Assess the morphology of the erythrocytes.
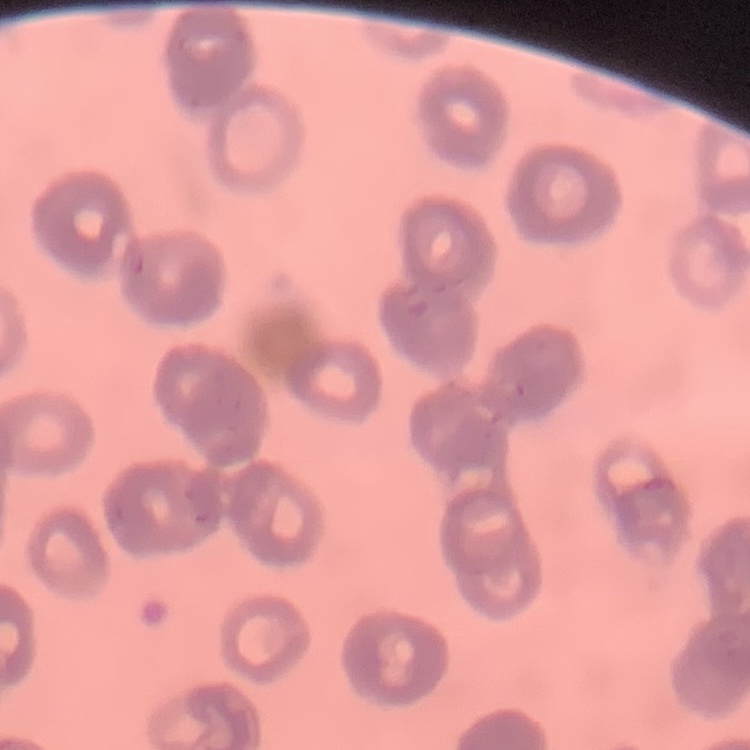
They show rouleaux formation.

image_type: square crop of a larger photomicrograph
preparation: thin blood film
stain: Field's or Giemsa